Report the malaria status of this cell.
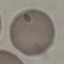
Uninfected.

Summary:
  - Capture: smartphone through the microscope eyepiece
  - Preparation: thin blood smear
  - Stain: Giemsa
  - Image type: automatically extracted cell patch, resized to 64 × 64 pixels